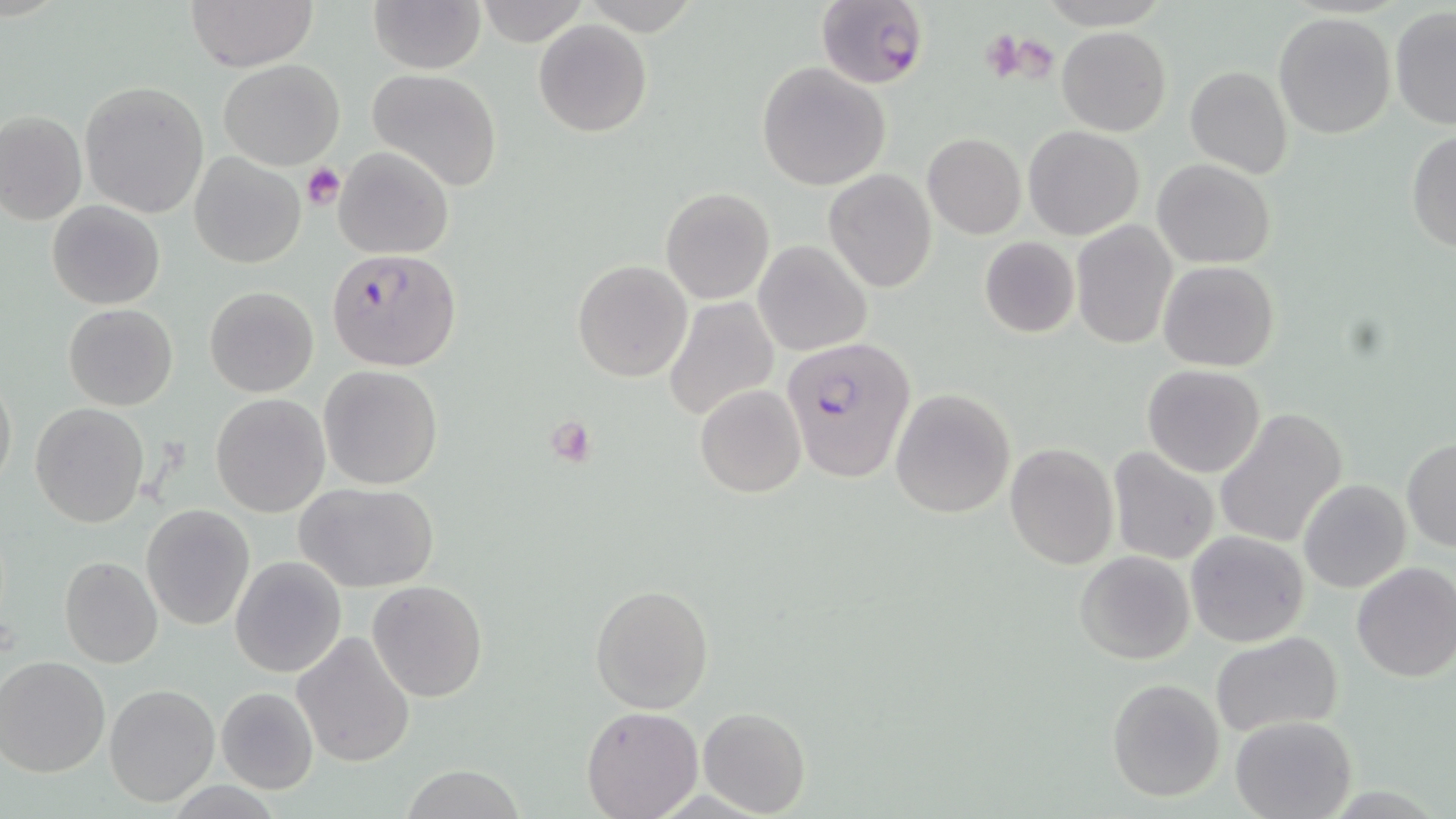

slide_level_diagnosis: Plasmodium falciparum
platelet_locations: 'approximate bounding boxes as named x1/y1/x2/y2 corners in pixels: (x1=980, y1=26, x2=1025, y2=84), (x1=991, y1=33, x2=1055, y2=83), (x1=301, y1=164, x2=345, y2=210), (x1=547, y1=416, x2=598, y2=469)'
plasmodium_falciparum_infected_red_blood_cell_locations: 'approximate bounding boxes as named x1/y1/x2/y2 corners in pixels: (x1=817, y1=0, x2=928, y2=89), (x1=325, y1=248, x2=461, y2=371), (x1=781, y1=335, x2=916, y2=483)'
image_size: 1456×819 pixels
magnification: 1000x
uninfected_red_blood_cell_locations: 'approximate bounding boxes as named x1/y1/x2/y2 corners in pixels: (x1=183, y1=0, x2=320, y2=70), (x1=367, y1=0, x2=484, y2=73), (x1=475, y1=0, x2=587, y2=47), (x1=1389, y1=6, x2=1456, y2=130), (x1=1272, y1=12, x2=1396, y2=139), (x1=533, y1=19, x2=652, y2=137), (x1=1057, y1=28, x2=1171, y2=136), (x1=218, y1=59, x2=345, y2=169), (x1=756, y1=62, x2=893, y2=190), (x1=1184, y1=65, x2=1293, y2=179), (x1=366, y1=68, x2=503, y2=191), (x1=79, y1=80, x2=210, y2=218), (x1=1, y1=110, x2=86, y2=224), (x1=1023, y1=125, x2=1144, y2=239), (x1=1406, y1=129, x2=1456, y2=255), (x1=922, y1=134, x2=1025, y2=239), (x1=333, y1=146, x2=452, y2=259), (x1=188, y1=154, x2=304, y2=268), (x1=1153, y1=159, x2=1276, y2=268), (x1=823, y1=169, x2=937, y2=293), (x1=661, y1=187, x2=775, y2=304), (x1=47, y1=200, x2=164, y2=310), (x1=1069, y1=221, x2=1178, y2=351), (x1=979, y1=236, x2=1080, y2=338), (x1=753, y1=240, x2=871, y2=356), (x1=571, y1=259, x2=692, y2=383), (x1=1159, y1=260, x2=1279, y2=372), (x1=205, y1=287, x2=319, y2=397), (x1=663, y1=296, x2=778, y2=423), (x1=64, y1=304, x2=178, y2=410), (x1=1142, y1=365, x2=1266, y2=477), (x1=319, y1=366, x2=443, y2=490), (x1=0, y1=370, x2=16, y2=491), (x1=696, y1=385, x2=806, y2=497), (x1=889, y1=388, x2=1015, y2=518), (x1=211, y1=393, x2=329, y2=517), (x1=30, y1=403, x2=150, y2=527), (x1=1214, y1=408, x2=1348, y2=550), (x1=1402, y1=437, x2=1455, y2=551), (x1=1005, y1=443, x2=1117, y2=568), (x1=1107, y1=449, x2=1219, y2=566), (x1=1298, y1=478, x2=1411, y2=592), (x1=292, y1=481, x2=441, y2=593), (x1=140, y1=504, x2=255, y2=631), (x1=1186, y1=530, x2=1310, y2=646), (x1=1075, y1=551, x2=1195, y2=664), (x1=228, y1=554, x2=347, y2=678), (x1=59, y1=556, x2=163, y2=668), (x1=1351, y1=563, x2=1456, y2=683), (x1=368, y1=580, x2=488, y2=701), (x1=589, y1=583, x2=714, y2=712), (x1=292, y1=630, x2=416, y2=768), (x1=1210, y1=632, x2=1344, y2=738), (x1=0, y1=655, x2=110, y2=778), (x1=1106, y1=678, x2=1226, y2=802), (x1=103, y1=682, x2=219, y2=806), (x1=216, y1=687, x2=318, y2=793), (x1=580, y1=706, x2=703, y2=819), (x1=699, y1=707, x2=810, y2=816), (x1=1230, y1=715, x2=1356, y2=819), (x1=395, y1=767, x2=525, y2=819)'
modality: optical microscopy
field_of_view: one of a larger specimen
preparation: thin blood film
stain: May-Grünwald-Giemsa